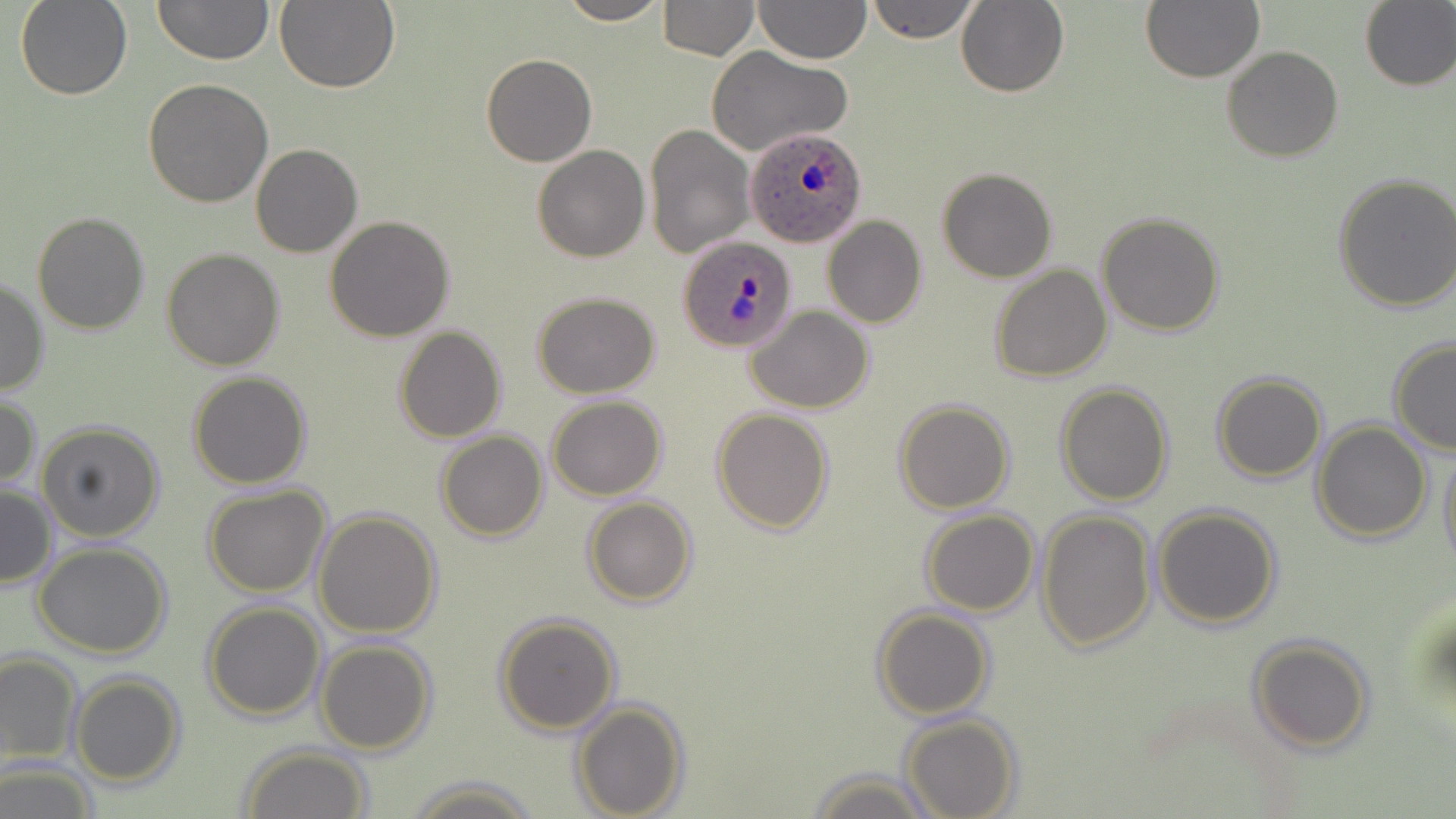

{
  "slide_level_diagnosis": "Plasmodium ovale",
  "preparation": "thin blood film",
  "image_size": "1456×819 pixels",
  "stain": "May-Grünwald-Giemsa",
  "modality": "optical microscopy",
  "plasmodium_ovale_infected_red_blood_cell_locations": "approximate bounding boxes as (x1,y1)-(x2,y2) corner pairs in pixels: (745,125)-(868,247), (678,234)-(798,353)",
  "magnification": "1000x",
  "uninfected_red_blood_cell_locations": "approximate bounding boxes as (x1,y1)-(x2,y2) corner pairs in pixels: (16,0)-(131,100), (153,0)-(273,67), (274,0)-(401,95), (555,0)-(670,25), (659,0)-(759,59), (753,0)-(871,65), (866,0)-(980,44), (1141,0)-(1265,83), (957,1)-(1070,97), (1359,1)-(1456,91), (1222,46)-(1343,162), (706,47)-(851,157), (481,53)-(597,167), (143,79)-(274,206), (644,122)-(755,259), (250,144)-(362,258), (532,145)-(650,262), (936,166)-(1058,282), (1333,172)-(1456,312), (31,210)-(152,335), (1096,212)-(1225,335), (325,215)-(455,340), (824,216)-(927,329), (162,247)-(285,370), (170,250)-(295,489), (990,265)-(1112,382), (0,275)-(49,397), (532,292)-(660,398), (747,306)-(875,414), (392,326)-(507,442), (1388,338)-(1456,455), (187,371)-(312,489), (1212,371)-(1327,482), (1054,383)-(1175,505), (0,394)-(40,491), (548,395)-(666,499), (894,398)-(1015,514), (712,408)-(834,533), (1310,420)-(1433,543), (36,421)-(165,542), (435,430)-(549,541), (1438,439)-(1456,571), (0,483)-(57,589), (203,485)-(331,597), (582,497)-(699,606), (1152,504)-(1282,629), (313,509)-(442,637), (1038,509)-(1156,653), (920,510)-(1039,616), (33,543)-(172,659), (202,600)-(326,720), (873,606)-(992,720), (493,612)-(622,735), (1247,635)-(1375,754), (314,639)-(437,754), (0,651)-(82,765), (70,674)-(187,786), (571,698)-(688,818), (899,713)-(1021,819), (239,745)-(372,819), (0,762)-(99,818), (809,768)-(936,819), (403,774)-(543,817)",
  "field_of_view": "one of a larger specimen"
}